Give the position of every leukocyte visible.
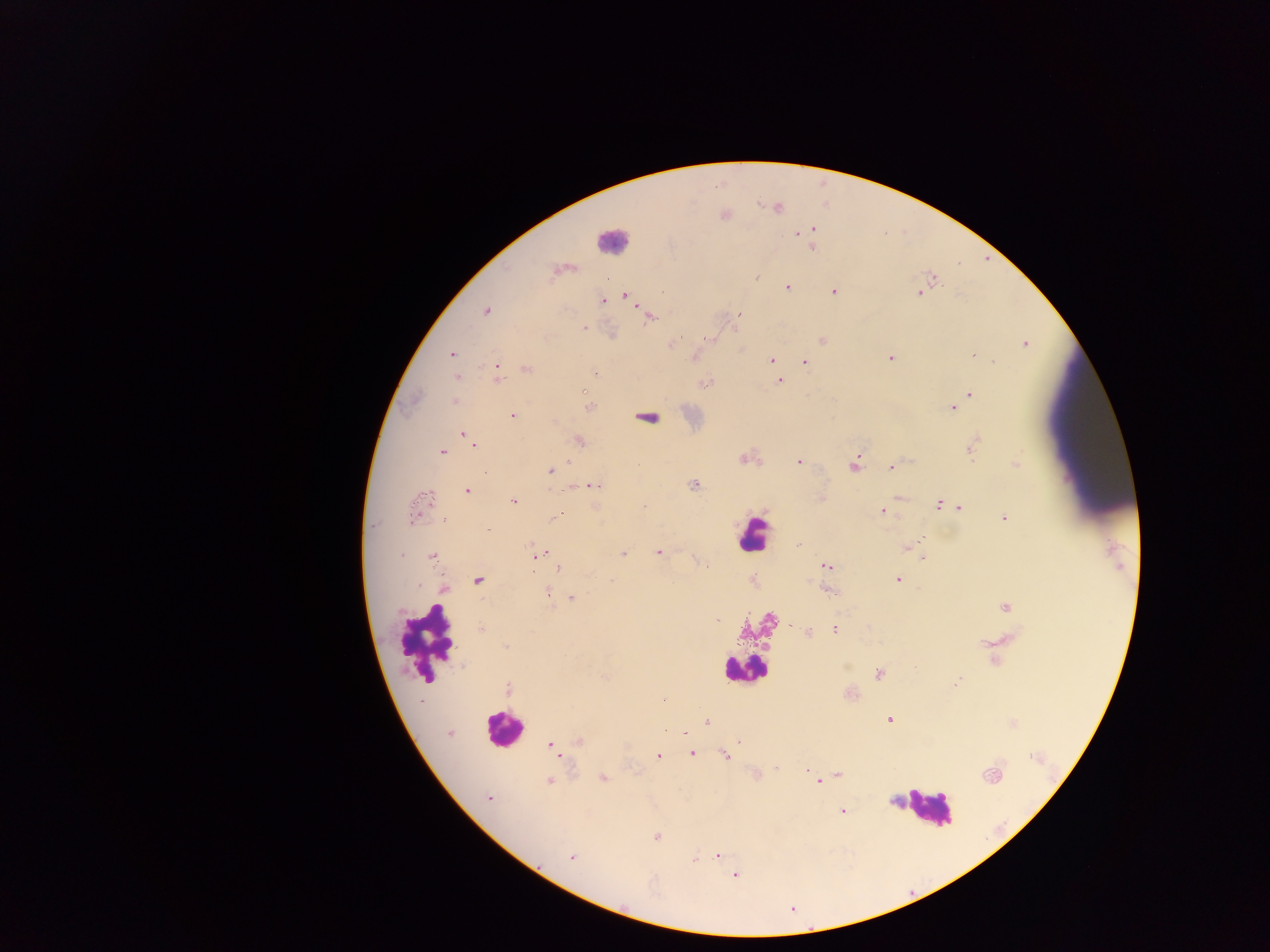

Approximate centers as x y in pixels.
Leukocytes: 612 238; 752 535; 425 642; 745 676; 503 729; 927 807.

Malaria parasite locations: 725 216; 814 228; 795 236; 812 249; 554 273; 757 278; 605 279; 931 279; 788 287; 834 292; 624 294; 919 295; 603 300; 485 312; 739 314; 650 316; 583 328; 821 339; 674 340; 1024 343; 452 355; 973 355; 770 358; 890 358; 993 360; 805 361; 495 367; 526 369; 595 372; 456 378; 780 381; 706 382; 971 393; 454 402; 953 407; 512 415; 647 417; 463 435; 579 440; 974 441; 473 448; 441 451; 970 452; 743 457; 798 461; 1015 463; 854 466; 892 467; 556 469; 693 485; 586 488; 467 490; 899 496; 822 498; 429 499; 513 502; 938 503; 959 507; 881 510; 556 515; 1004 517; 445 520; 919 536; 799 544; 906 547; 658 551; 623 552; 432 557; 534 558; 923 558; 704 563; 824 566; 559 567; 897 580; 477 581; 611 581; 753 582; 419 586; 827 589; 548 590; 443 591; 572 598; 1005 607; 718 621; 769 621; 834 629; 982 643; 505 645; 444 654; 992 661; 847 667; 879 674; 606 676; 957 682; 507 688; 662 700; 420 702; 890 720; 707 721; 1010 725; 685 732; 450 734; 577 741; 549 743; 691 753; 658 756; 725 756; 559 757; 777 769; 804 770; 755 774; 992 774; 838 775; 603 780; 550 782; 819 783; 489 797; 893 802; 844 811; 657 835; 718 853; 573 858; 694 859; 736 877. Thick blood film. Sample from Ghana. Mobile-phone photograph taken through the microscope. Image is 1270×952 pixels. Single field of view.